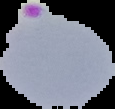
Result: malaria parasites identified. Segmented cell region on a black background. From a thin blood film. Image is 115×109 pixels.